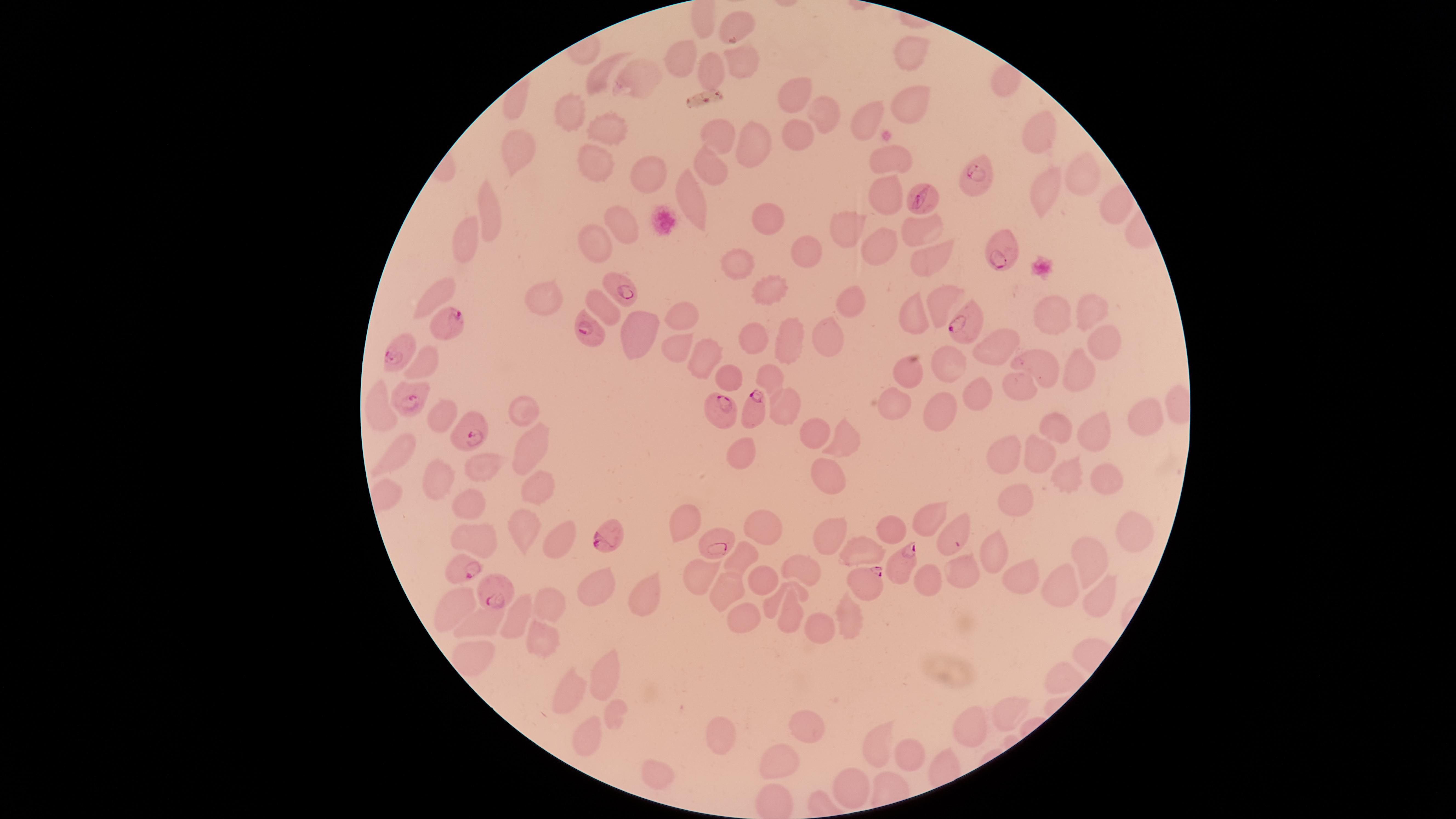

parasitized red blood cells = approximate marker points as (x, y) in pixels: (978, 174), (921, 200), (1001, 253), (625, 290), (447, 320), (965, 327), (592, 332), (398, 350), (405, 397), (752, 407), (723, 412), (474, 434), (614, 534), (954, 537), (719, 543), (904, 565), (463, 568), (867, 584), (500, 589)
field of view = single
species = Plasmodium falciparum
image size = 1456×819 pixels
uninfected red blood cells = approximate marker points as (x, y) in pixels: (912, 52), (682, 55), (736, 62), (710, 70), (598, 75), (641, 76), (795, 92), (909, 104), (562, 119), (818, 119), (869, 119), (604, 129), (721, 134), (1038, 135), (797, 136), (753, 144), (514, 155), (886, 157), (592, 163), (1083, 163), (713, 169), (656, 176), (1052, 192), (883, 193), (689, 203), (1112, 206), (768, 214), (487, 218), (624, 223), (849, 226), (917, 227), (469, 232), (599, 245), (807, 248), (872, 248), (930, 256), (741, 260), (769, 287), (435, 293), (548, 294), (938, 298), (849, 305), (1090, 308), (603, 310), (684, 311), (913, 312), (1049, 312), (637, 334), (827, 334), (1105, 338), (754, 340), (790, 342), (1005, 343), (676, 348), (704, 360), (951, 363), (1044, 364), (1078, 366), (423, 367), (731, 373), (914, 373), (769, 375), (1020, 382), (980, 391), (897, 400), (790, 403), (378, 404), (937, 406), (526, 413), (1145, 415), (440, 419), (1064, 429), (1099, 432), (815, 434), (847, 440), (399, 446), (531, 448), (740, 453), (1007, 453), (1039, 454), (481, 463), (823, 472), (1065, 479), (1106, 479), (439, 480), (537, 484), (1015, 495), (465, 501), (687, 521), (929, 521), (758, 525), (521, 526), (890, 532), (828, 534), (1135, 535), (475, 539), (558, 544), (861, 550), (1092, 553), (738, 557), (995, 562), (806, 570), (963, 578), (699, 580), (762, 580), (929, 581), (1023, 585), (1057, 585), (595, 589), (799, 589), (728, 593), (644, 594), (1098, 595), (551, 600), (456, 603), (790, 607), (513, 611), (853, 613), (742, 617), (480, 621), (817, 626), (538, 639), (472, 647), (1060, 673), (605, 676), (570, 692), (1008, 709), (616, 715), (806, 723), (968, 725), (721, 729), (585, 732), (879, 742), (912, 749), (781, 757), (656, 770), (848, 785)
stain = Giemsa
presence = malaria parasites seen
capture = smartphone photograph through the microscope eyepiece
visible region = circular
preparation = thin smear of blood